Point out each malaria parasite.
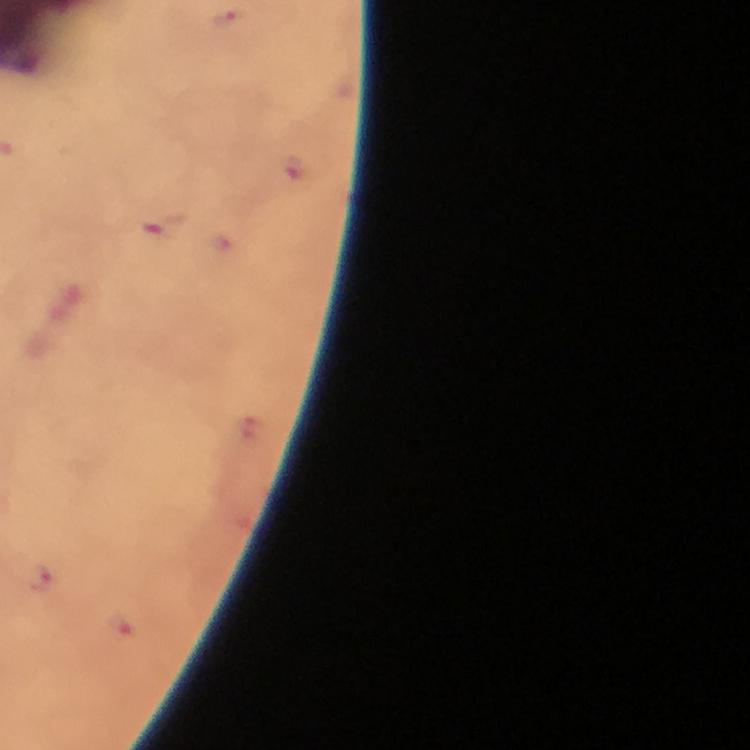
Approximate centers as (x, y) in pixels.
Malaria parasites: (291, 169), (163, 224), (38, 577), (121, 630).

stain = Giemsa
magnification = 100x
context = from a diagnostic examination for malaria
immersion oil = applied
cropped from = one field of view
capture = smartphone mounted on the microscope
preparation = thick blood film
image size = 750×750 pixels